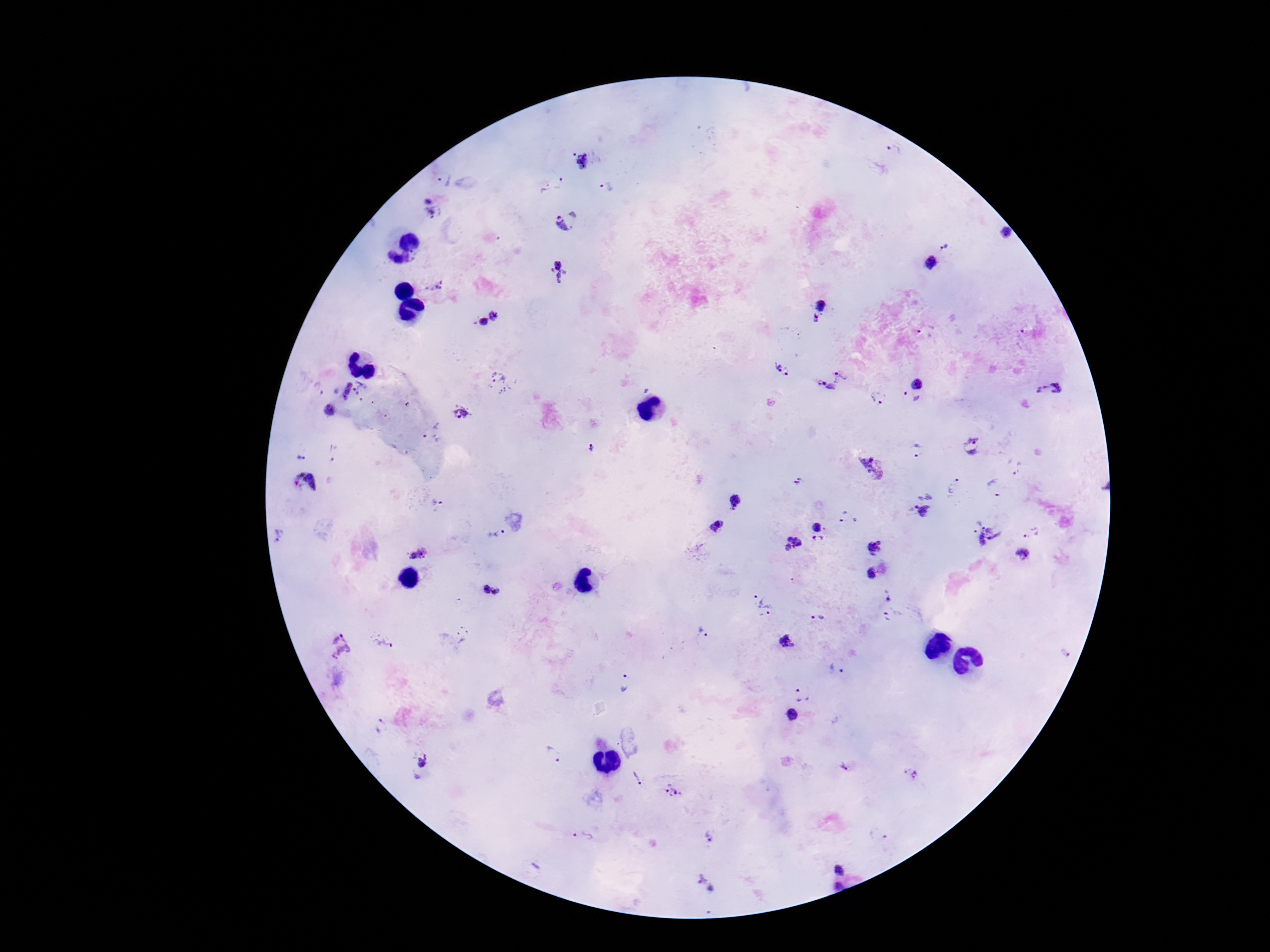
Approximate centers as (x, y) in pixels. Plasmodium parasite locations: (894, 149), (580, 161), (443, 178), (561, 183), (545, 188), (606, 188), (432, 209), (574, 213), (562, 225), (1007, 234), (945, 246), (930, 262), (558, 272), (432, 287), (821, 306), (496, 314), (815, 321), (480, 323), (924, 329), (776, 366), (788, 372), (840, 374), (501, 381), (918, 384), (317, 388), (341, 388), (826, 388), (1059, 388), (363, 389), (1041, 389), (877, 399), (908, 400), (373, 403), (408, 405), (329, 410), (461, 413), (382, 415), (433, 433), (973, 445), (917, 449), (592, 451), (335, 453), (301, 456), (871, 467), (1018, 469), (304, 484), (798, 484), (953, 485), (994, 488), (733, 501), (436, 504), (922, 511), (849, 518), (716, 525), (816, 527), (498, 534), (1031, 534), (987, 536), (279, 537), (818, 540), (793, 544), (873, 547), (420, 554), (1024, 555), (870, 574), (492, 590), (888, 595), (458, 602), (760, 604), (819, 619), (888, 619), (462, 634), (702, 634), (381, 642), (787, 642), (339, 646), (1066, 653), (836, 669), (625, 683), (803, 693), (793, 716), (381, 727), (555, 755), (846, 767), (419, 768), (908, 773), (638, 777), (674, 791), (583, 836), (710, 836), (842, 867), (706, 884), (837, 886). Patient malaria status: infected. Thick blood smear. Single field of view. Image is 1270×952 pixels. Giemsa-stained preparation. 100x magnification. Photographed through the microscope eyepiece with a smartphone camera.